Give the position of every Plasmodium parasite visible.
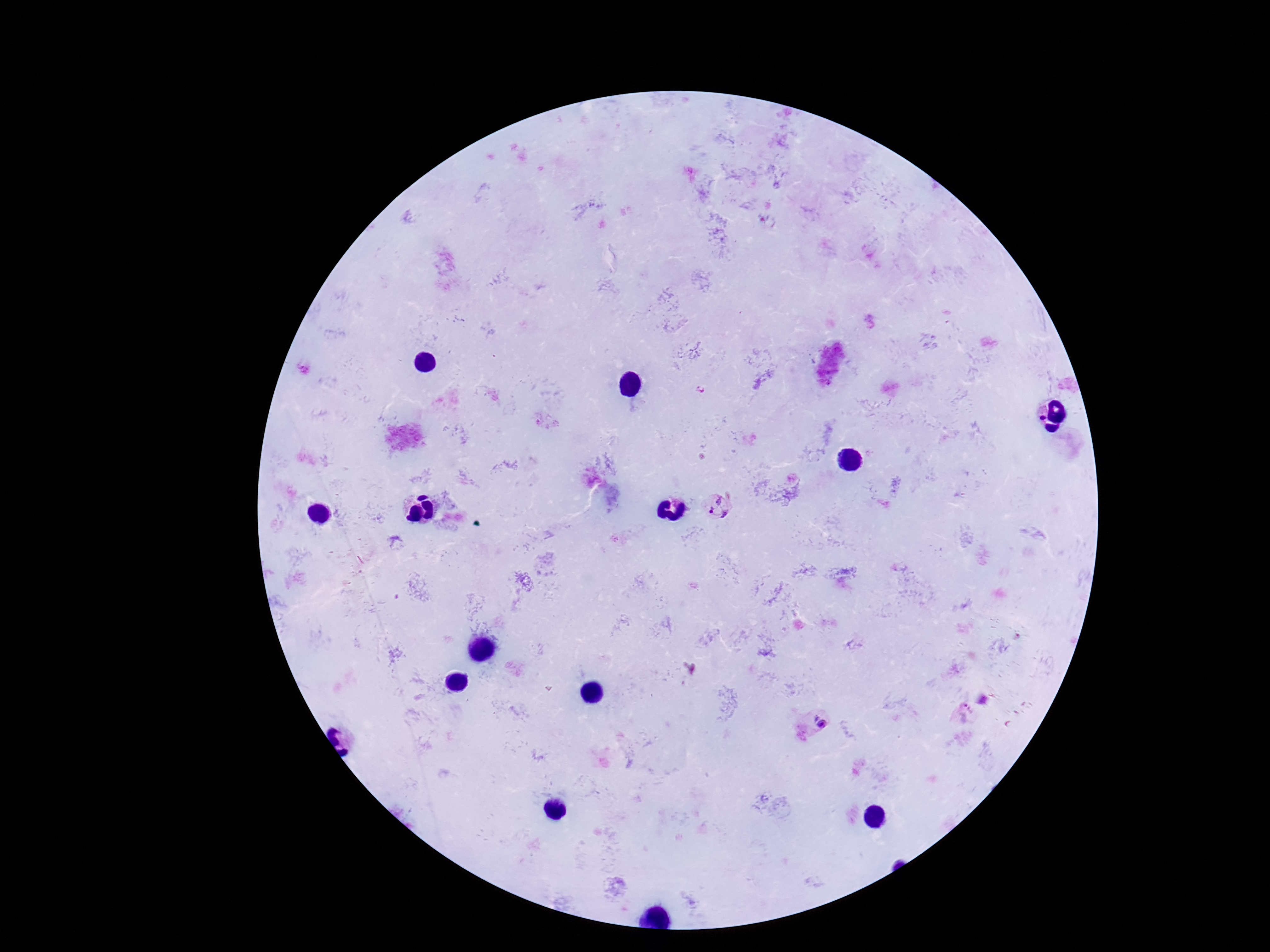
Approximate centers as [x, y] in pixels.
Plasmodium parasites: [718, 504], [964, 714], [817, 722].

Giemsa-stained preparation. Single field of view. Smartphone photograph taken through the microscope eyepiece. 100x magnification. Thick blood smear. Patient malaria status: positive. Image is 1270×952 pixels.